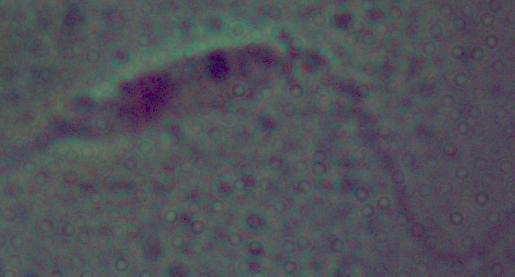
Photomicrograph. Captured at 1000x magnification. A Leishmania parasite is shown.